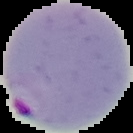
From a thin blood film. Cell region segmented out of the field of view; the surrounding area is masked to black. Result: Plasmodium parasites identified. Image is 133×133 pixels.